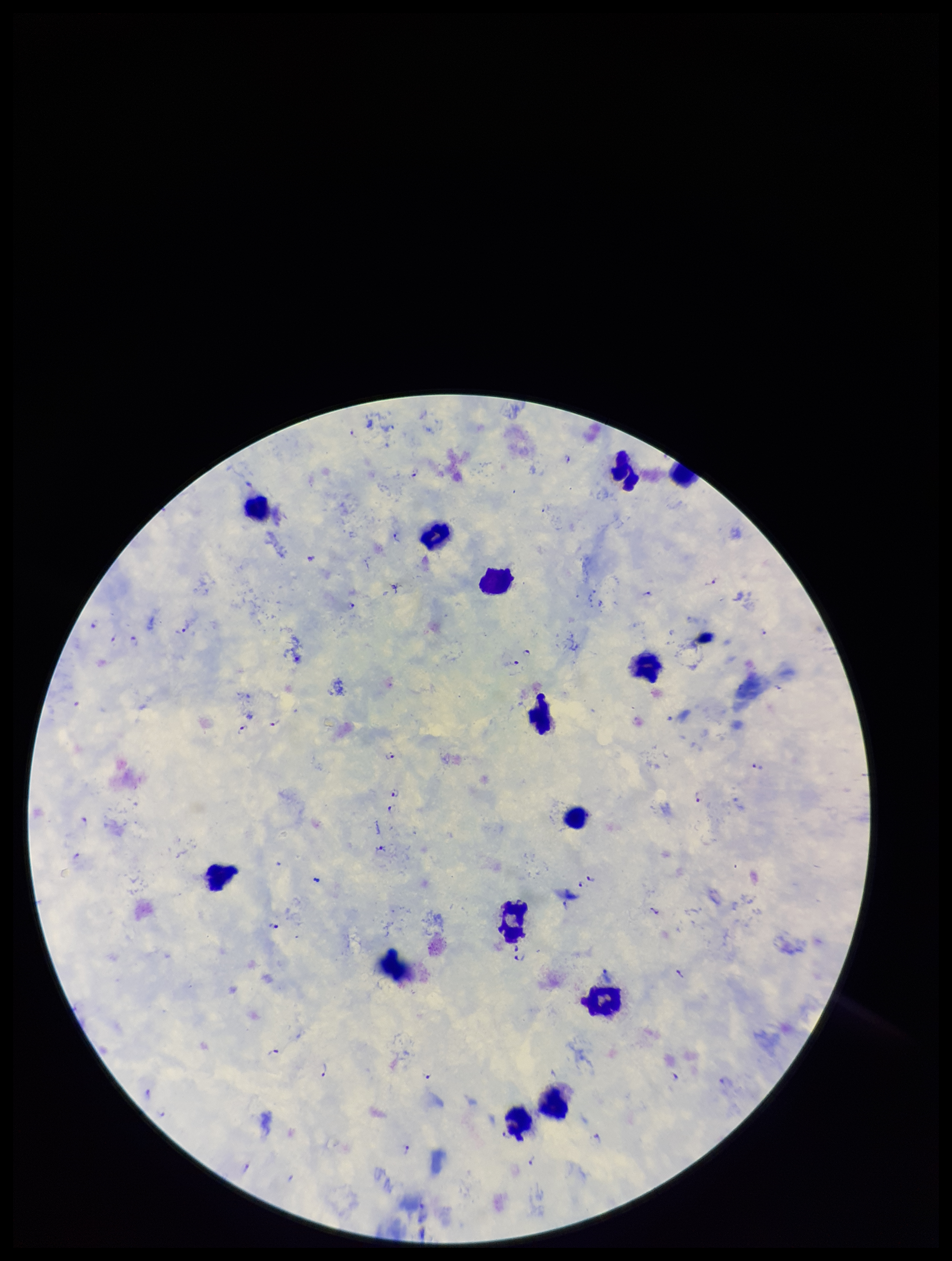

{
  "patient_malaria_status": "positive",
  "capture": "smartphone photograph through the microscope eyepiece",
  "species_reported_for_this_patient": "Plasmodium falciparum",
  "parasite_count": 39,
  "stain": "Giemsa",
  "field_of_view": "single",
  "image_size": "952×1261 pixels",
  "plasmodium_parasites": "seen",
  "preparation": "thick",
  "leukocyte_count": 14
}